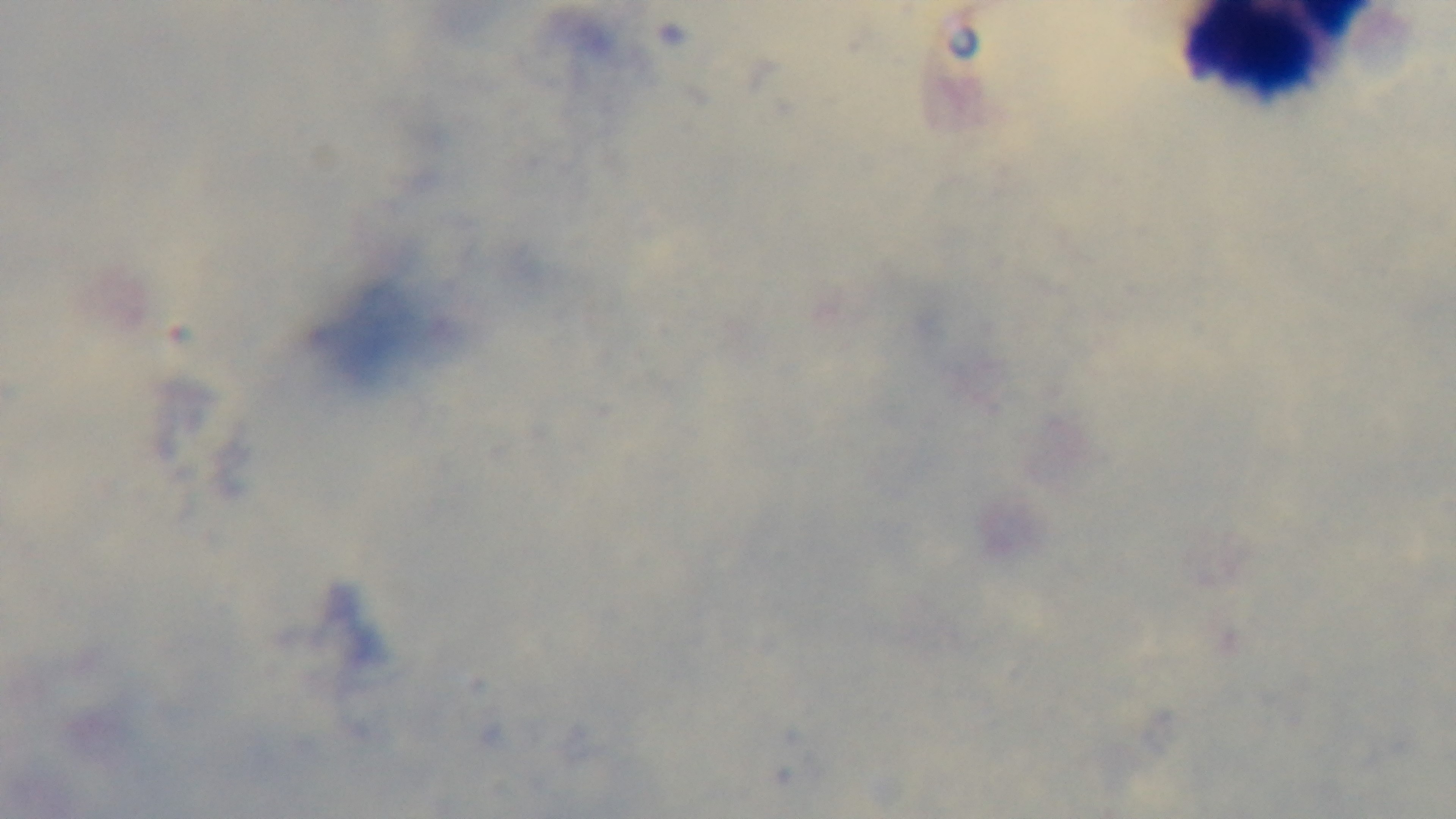

Summary:
  - Preparation: thick smear
  - Stain: Giemsa
  - Objective: 100x oil immersion
  - Capture: mounted 4K digital camera
  - Field of view: single
  - Malaria status: negative
  - Modality: light microscopy